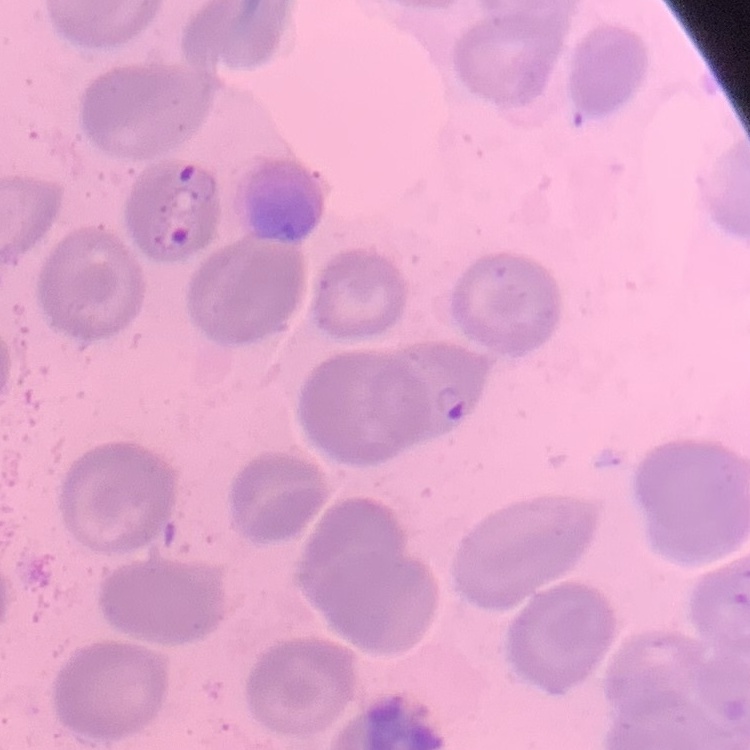
Summary:
  - Red blood cell morphology: no rouleaux formation
  - Stain: Field's or Giemsa
  - Image type: square crop of a larger photomicrograph
  - Preparation: thin blood film